Describe the morphology of the red blood cells.
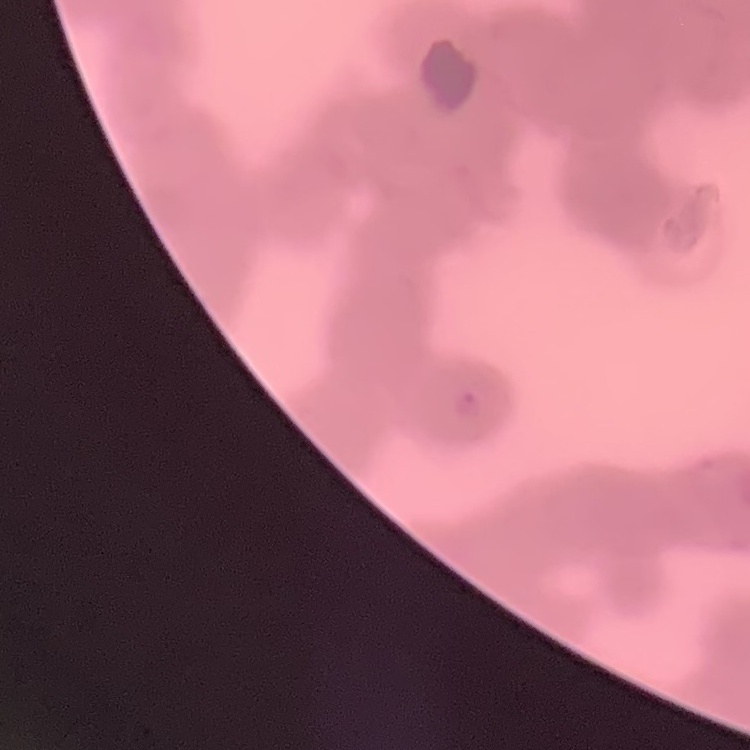

Rouleaux formation.

image_type: one tile cut from a larger photomicrograph
preparation: thin blood smear
stain: Field's or Giemsa